Identify the parasite.
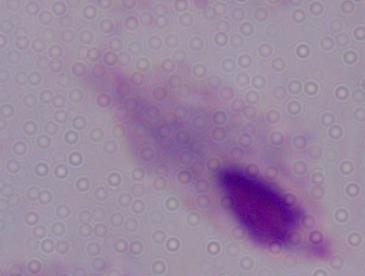
This is a trichomonad.

1000x magnification. Photomicrograph.